Locate every Plasmodium parasite.
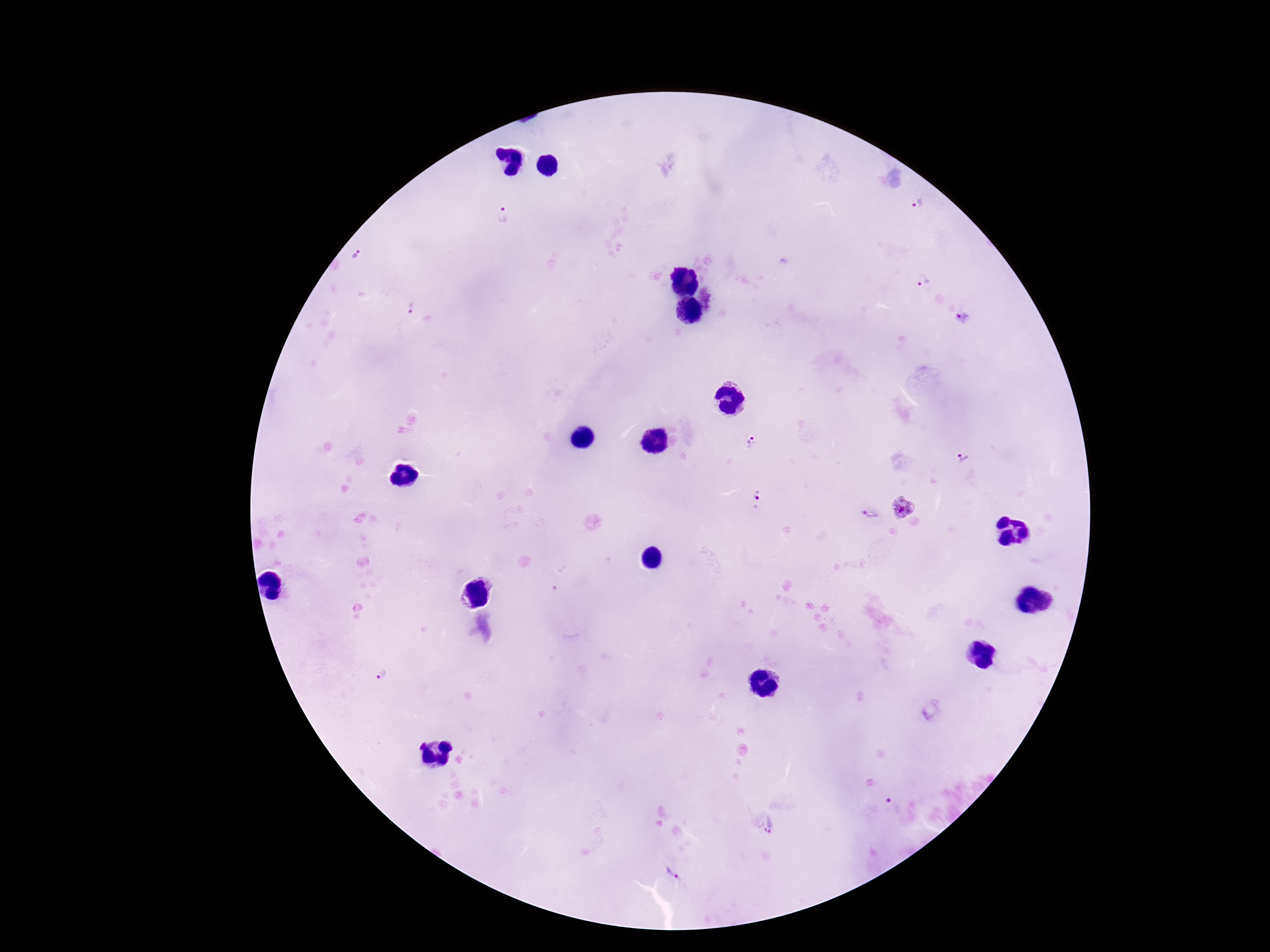
Approximate object centers, in pixels from the top-left corner.
Plasmodium parasites: (x=919, y=205), (x=504, y=214), (x=357, y=254), (x=922, y=280), (x=409, y=306), (x=963, y=317), (x=752, y=442), (x=964, y=459), (x=758, y=496), (x=904, y=508), (x=869, y=514), (x=383, y=674), (x=771, y=828), (x=673, y=873).

Smartphone photograph taken through the microscope eyepiece. Patient malaria status: positive. Giemsa stain. 100x magnification. Thick blood film. Image is 1270×952 pixels. One field from this slide.